Name the parasite shown.
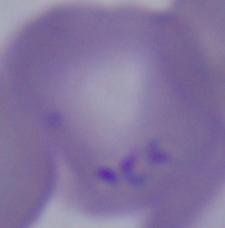

This is Babesia.

Summary:
  - Magnification: 1000x
  - Modality: photomicrograph